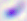

magnification = 400x
modality = micrograph
identification = Toxoplasma gondii